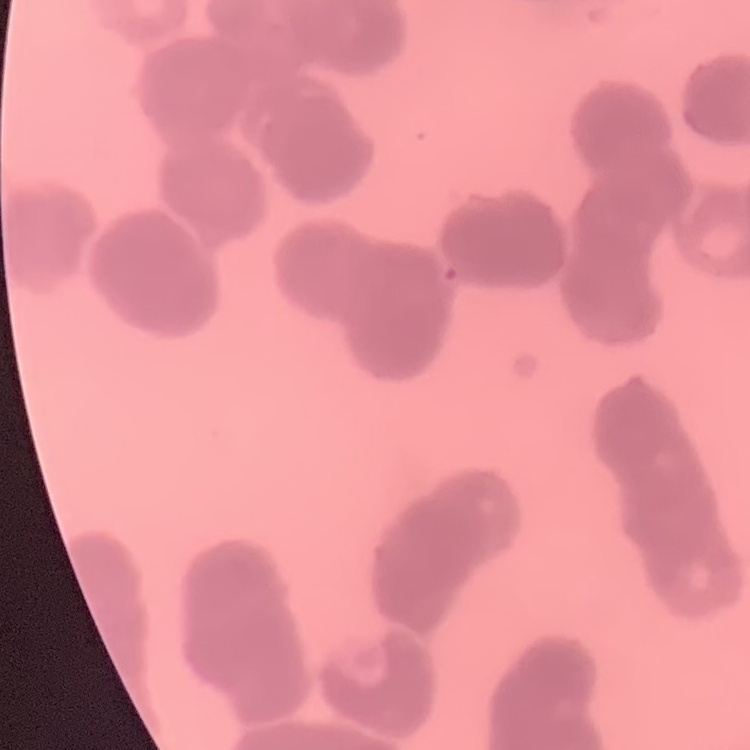 The red blood cells exhibit rouleaux formation. Thin peripheral smear. Field's or Giemsa stain. Square crop of a larger photomicrograph.